Give the extent of all Plasmodium malariae-infected red blood cells.
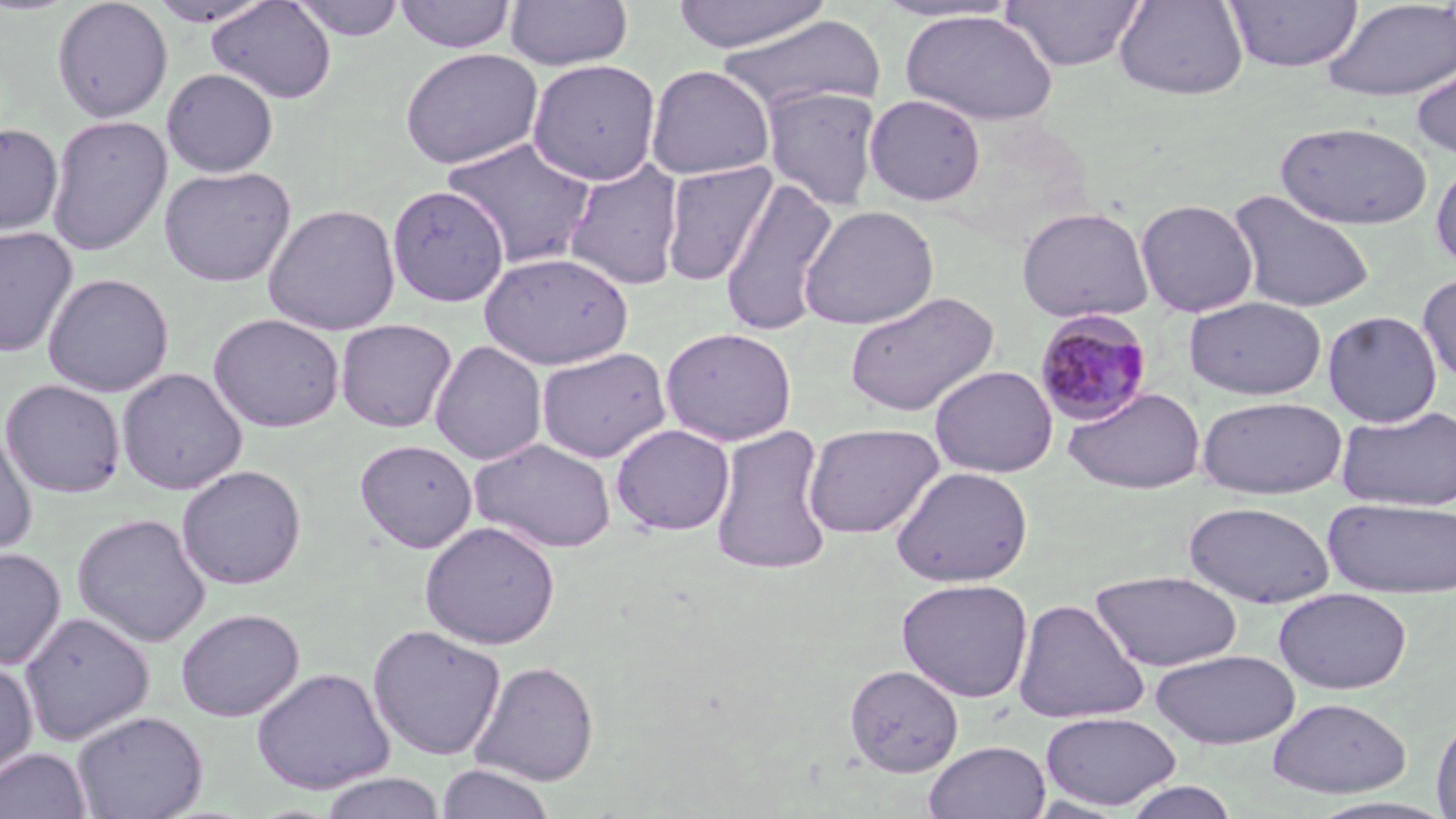

Approximate bounding boxes as [x1, y1, x2, y2] in pixels.
Plasmodium malariae-infected red blood cells: [1033, 310, 1154, 428].

Summary:
  - Uninfected red blood cell locations: [52, 0, 173, 123], [147, 0, 276, 28], [206, 0, 336, 104], [290, 0, 406, 41], [393, 0, 517, 53], [504, 0, 633, 71], [669, 0, 831, 52], [871, 0, 1021, 25], [1001, 0, 1146, 72], [1113, 0, 1248, 100], [1223, 0, 1364, 74], [1321, 0, 1456, 102], [899, 9, 1058, 126], [716, 14, 884, 119], [399, 47, 543, 170], [1411, 52, 1456, 163], [527, 59, 662, 186], [646, 64, 774, 180], [161, 68, 279, 178], [762, 85, 883, 210], [864, 94, 986, 206], [46, 115, 172, 256], [1275, 120, 1433, 231], [0, 123, 63, 238], [442, 138, 598, 269], [1430, 158, 1456, 275], [563, 159, 685, 291], [660, 161, 777, 287], [158, 165, 296, 287], [718, 177, 838, 338], [387, 185, 509, 306], [1227, 188, 1375, 313], [1135, 199, 1259, 317], [263, 203, 401, 336], [798, 205, 939, 330], [1016, 206, 1154, 324], [0, 226, 78, 359], [478, 251, 634, 369], [1417, 271, 1456, 386], [43, 272, 174, 397], [844, 290, 1000, 418], [1183, 296, 1327, 400], [1322, 310, 1443, 428], [208, 312, 345, 432], [335, 318, 457, 433], [660, 327, 797, 446], [429, 340, 547, 465], [535, 347, 672, 463], [929, 364, 1058, 478], [116, 367, 247, 495], [1, 379, 125, 498], [1063, 387, 1206, 494], [1196, 396, 1348, 500], [1337, 405, 1456, 512], [802, 422, 944, 539], [610, 423, 734, 536], [709, 425, 834, 575], [0, 427, 37, 557], [468, 438, 617, 554], [354, 439, 477, 552], [176, 464, 307, 590], [890, 466, 1033, 587], [1323, 496, 1456, 599], [1183, 501, 1336, 608], [72, 512, 211, 648], [419, 520, 561, 650], [0, 547, 66, 669], [1089, 570, 1244, 672], [896, 578, 1034, 703], [1274, 587, 1412, 694], [1013, 598, 1150, 725], [176, 608, 304, 722], [19, 610, 154, 746], [367, 624, 506, 761], [1150, 648, 1301, 749], [0, 657, 38, 782], [470, 661, 600, 786], [844, 663, 964, 777], [252, 667, 394, 795], [1267, 697, 1412, 799], [71, 710, 207, 819], [1040, 711, 1182, 810], [1430, 711, 1456, 818], [923, 740, 1051, 819], [0, 747, 93, 819], [436, 763, 556, 819], [318, 772, 446, 819], [1120, 781, 1240, 819]
  - Slide-level diagnosis: Plasmodium malariae
  - Field of view: one of a larger specimen
  - Preparation: thin blood smear
  - Stain: May-Grünwald-Giemsa
  - Modality: optical microscopy
  - Image size: 1456×819 pixels
  - Magnification: 1000x